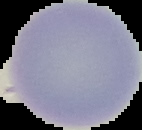

Malaria status: uninfected. Image is 142×130 pixels. From a thin blood film. Segmented cell region on a black background.